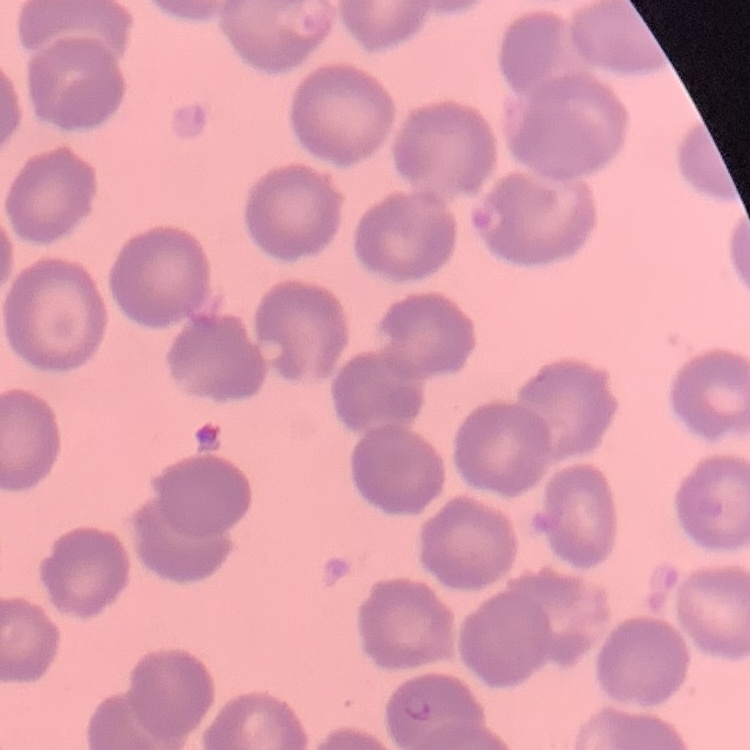 The erythrocytes exhibit no rouleaux formation. Thin peripheral smear. Field's or Giemsa stain. One tile cut from a larger photomicrograph.